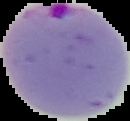

malaria_status: parasitized
image_type: cell region segmented out of the field of view; surrounding area masked to black
preparation: thin blood film
image_size: 130×121 pixels